Locate every blood parasite and identify its species.
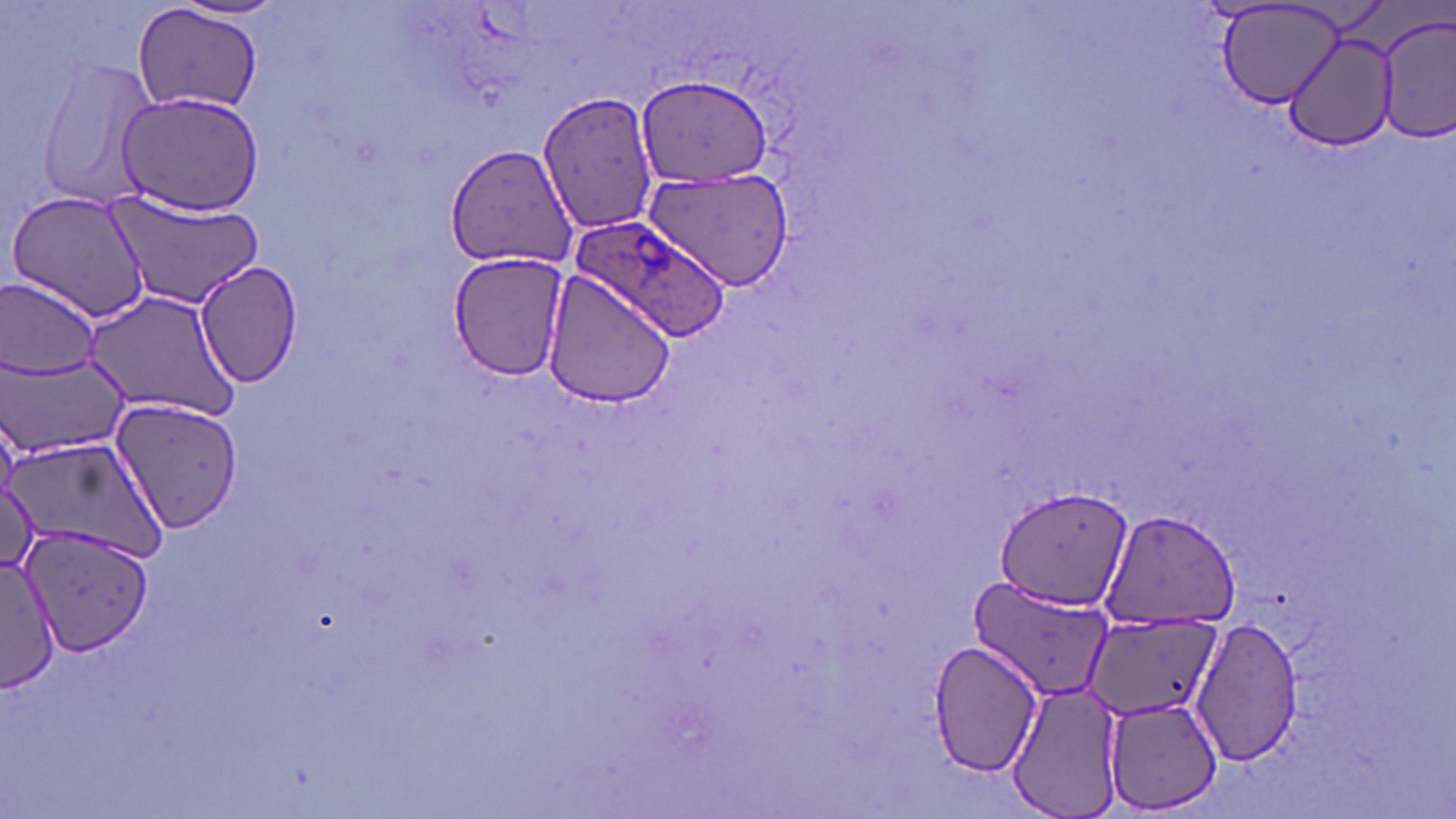
Approximate bounding boxes as (x1, y1, x2, y2) in pixels.
Plasmodium ovale-infected red blood cells: (568, 214, 733, 343).
No Plasmodium falciparum, Plasmodium malariae, Plasmodium vivax, Babesia divergens, or Trypanosoma brucei observed.

slide_level_diagnosis: Plasmodium ovale
preparation: thin blood film
stain: May-Grünwald-Giemsa
modality: optical microscopy
image_size: 1456×819 pixels
field_of_view: one of a larger specimen
magnification: 1000x
uninfected_red_blood_cell_locations: 'approximate bounding boxes as (x1, y1, x2, y2) in pixels: (172, 1, 292, 24), (1214, 2, 1348, 110), (132, 3, 263, 116), (1376, 11, 1456, 143), (1282, 30, 1396, 149), (28, 53, 162, 213), (633, 74, 777, 186), (538, 89, 660, 236), (114, 90, 266, 216), (445, 144, 579, 269), (643, 169, 795, 291), (6, 187, 153, 326), (102, 188, 267, 310), (448, 250, 573, 380), (195, 260, 305, 388), (541, 271, 678, 408), (0, 274, 105, 380), (83, 287, 242, 419), (4, 354, 130, 461), (108, 396, 246, 537), (5, 436, 161, 562), (1, 479, 39, 574), (994, 486, 1131, 611), (1100, 508, 1245, 630), (21, 526, 153, 658), (0, 551, 60, 693), (968, 577, 1111, 703), (1090, 614, 1213, 719), (1188, 616, 1303, 767), (926, 638, 1044, 777), (1006, 679, 1124, 819), (1103, 700, 1225, 814)'